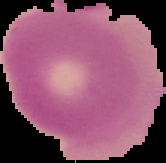
Result: negative for malaria parasites. The area outside the segmented cell region is set to black. From a thin blood film. Image is 166×163 pixels.